Locate and identify every blood parasite.
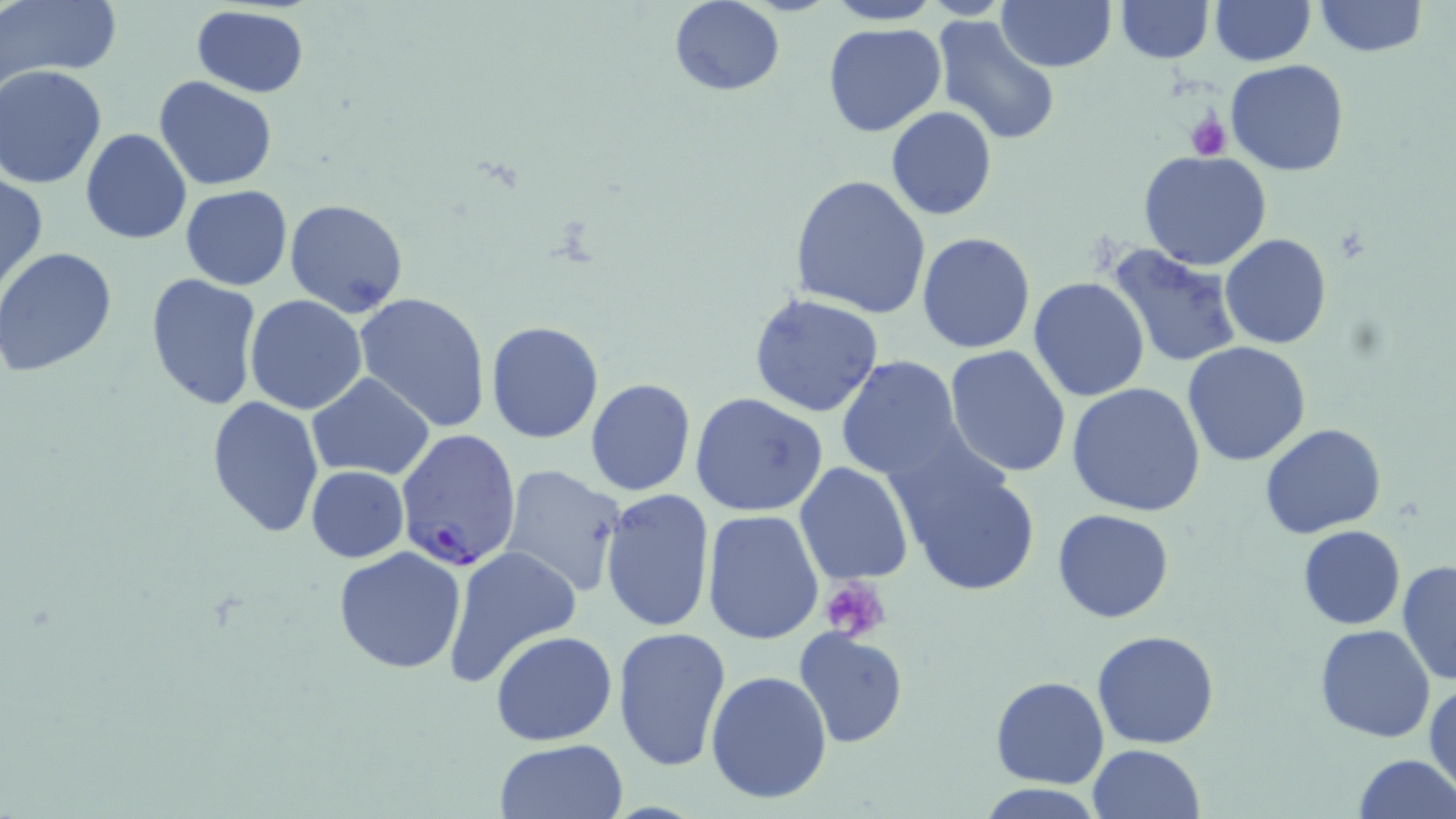

Approximate bounding boxes as (x1,y1)-(x2,y2) corner pairs in pixels.
Plasmodium falciparum-infected red blood cells: (394,427)-(523,572).
No Plasmodium ovale, Plasmodium malariae, Plasmodium vivax, Babesia divergens, or Trypanosoma brucei observed.

{
  "slide_level_diagnosis": "Plasmodium falciparum",
  "uninfected_red_blood_cell_locations": "approximate bounding boxes as (x1,y1)-(x2,y2) corner pairs in pixels: (3,0)-(122,81), (826,0)-(943,26), (996,0)-(1115,71), (1116,0)-(1213,62), (1314,0)-(1425,56), (668,1)-(783,95), (1209,1)-(1313,66), (190,5)-(309,97), (932,13)-(1064,147), (822,21)-(947,137), (1224,59)-(1351,178), (1,66)-(107,187), (152,77)-(278,191), (886,107)-(997,220), (79,128)-(192,245), (1138,151)-(1273,272), (0,171)-(47,295), (788,175)-(931,319), (180,185)-(293,289), (285,198)-(412,318), (917,231)-(1035,353), (1221,234)-(1333,350), (1105,242)-(1243,369), (0,248)-(121,379), (145,272)-(264,410), (1027,277)-(1151,404), (352,291)-(494,433), (749,293)-(884,417), (244,295)-(368,414), (485,319)-(604,444), (1183,341)-(1311,467), (944,345)-(1072,480), (837,355)-(964,481), (308,374)-(434,479), (585,378)-(696,496), (1065,383)-(1208,518), (690,393)-(828,517), (205,396)-(326,540), (1260,423)-(1387,539), (883,439)-(1042,601), (794,461)-(913,585), (498,463)-(627,597), (305,466)-(409,563), (601,488)-(715,636), (1052,508)-(1176,623), (701,509)-(824,646), (1297,525)-(1404,629), (332,546)-(468,675), (441,547)-(582,690), (1396,560)-(1455,686), (1315,624)-(1437,744), (612,626)-(733,771), (792,628)-(908,748), (1092,628)-(1221,749), (490,630)-(618,745), (706,669)-(833,805), (990,676)-(1109,788), (1426,681)-(1456,796), (496,739)-(626,819), (1087,744)-(1205,819), (1353,753)-(1456,819), (974,784)-(1109,818)",
  "preparation": "thin blood film",
  "magnification": "1000x",
  "image_size": "1456×819 pixels",
  "modality": "light microscopy",
  "stain": "May-Grünwald-Giemsa",
  "platelet_locations": "approximate bounding boxes as (x1,y1)-(x2,y2) corner pairs in pixels: (1185,113)-(1231,160), (819,579)-(891,643)",
  "field_of_view": "one of a larger specimen"
}